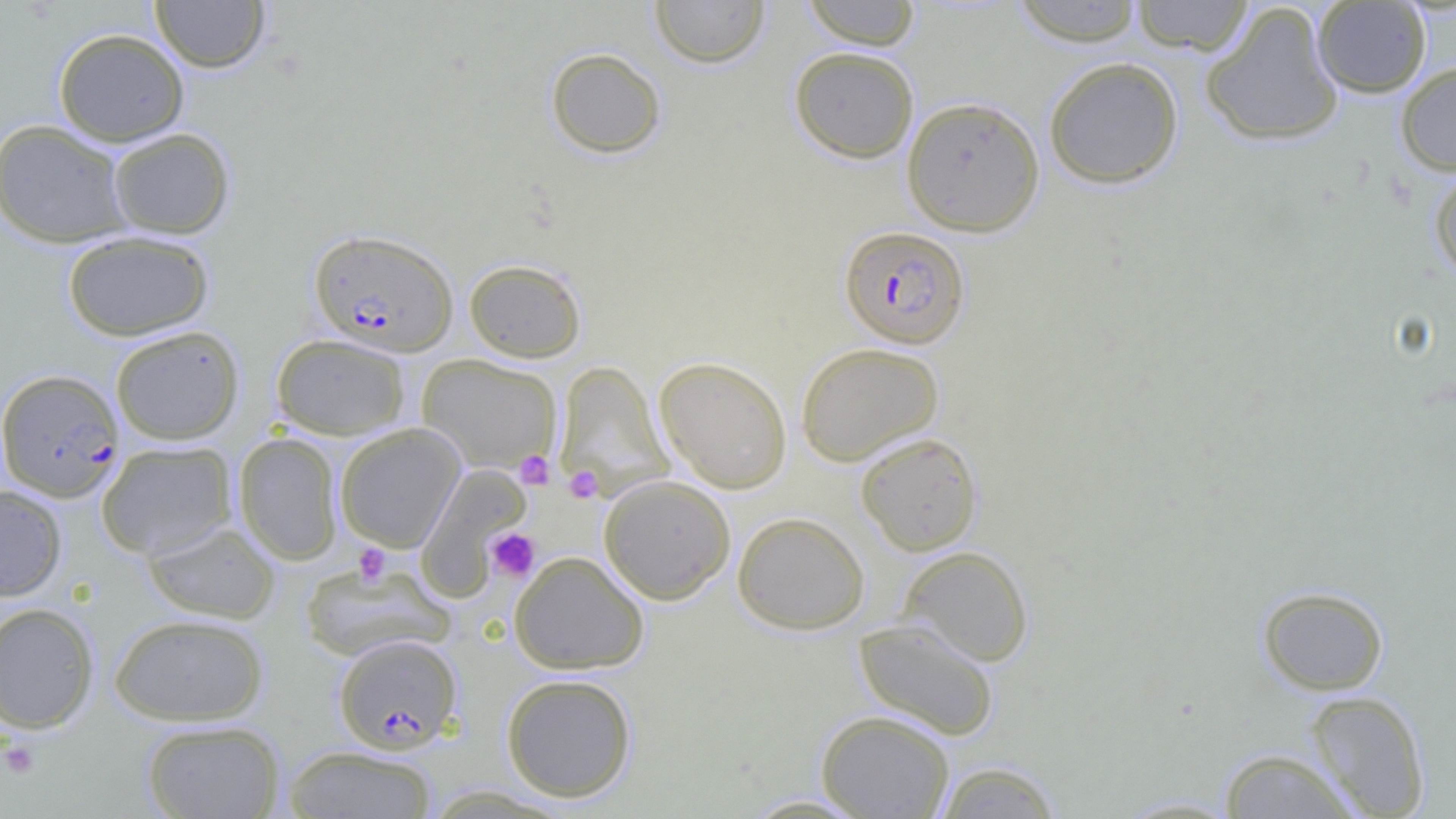

slide-level diagnosis = Plasmodium falciparum
uninfected red blood cell locations = approximate bounding boxes as [x1, y1, x2, y2] in pixels: [150, 0, 270, 73], [649, 0, 770, 68], [800, 0, 922, 49], [1129, 0, 1255, 55], [1009, 1, 1146, 46], [1312, 1, 1432, 98], [1199, 2, 1345, 148], [53, 27, 190, 146], [789, 46, 920, 163], [545, 47, 666, 159], [1043, 56, 1184, 189], [1395, 61, 1456, 175], [900, 95, 1045, 237], [0, 119, 133, 249], [106, 127, 236, 239], [1427, 163, 1456, 281], [62, 230, 214, 341], [464, 258, 587, 363], [110, 325, 245, 445], [271, 334, 411, 440], [795, 341, 944, 466], [417, 354, 561, 474], [654, 355, 793, 494], [554, 360, 673, 501], [335, 424, 465, 552], [233, 432, 344, 565], [855, 432, 983, 555], [96, 441, 237, 559], [414, 465, 531, 599], [599, 475, 736, 605], [0, 485, 67, 601], [732, 511, 870, 634], [143, 519, 280, 624], [898, 545, 1034, 666], [509, 551, 649, 674], [298, 560, 452, 662], [1257, 585, 1389, 695], [0, 602, 99, 733], [109, 613, 268, 726], [853, 618, 1001, 741], [501, 673, 638, 802], [1305, 690, 1431, 818], [816, 709, 955, 819], [140, 719, 285, 819], [282, 745, 438, 818], [1218, 747, 1362, 818], [932, 760, 1064, 818], [736, 793, 877, 817], [1112, 793, 1244, 818]
Plasmodium falciparum-infected red blood cell locations = approximate bounding boxes as [x1, y1, x2, y2] in pixels: [838, 225, 970, 349], [308, 227, 459, 357], [0, 368, 125, 501], [333, 633, 462, 753]
preparation = thin blood film
field of view = one of a larger specimen
modality = light microscopy
image size = 1456×819 pixels
platelet locations = approximate bounding boxes as [x1, y1, x2, y2] in pixels: [513, 450, 555, 490], [564, 466, 603, 503], [485, 528, 540, 583], [354, 544, 391, 586], [1, 739, 41, 778]
magnification = 1000x